Identify the preparation type.
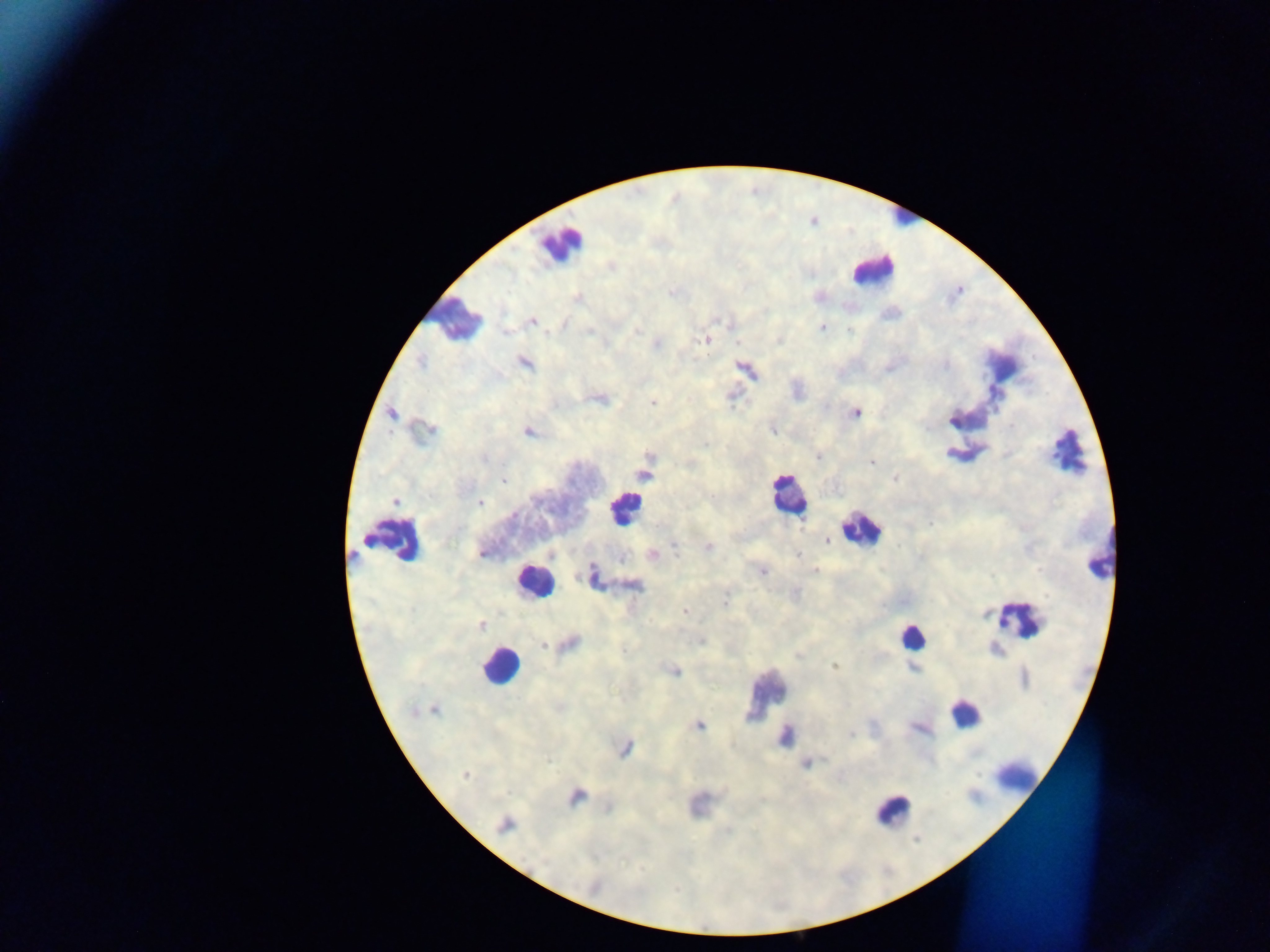

Thick blood film.

Approximate centers as (x, y) in pixels. Leukocyte locations: (554, 244), (864, 274), (455, 320), (1066, 454), (786, 488), (866, 534), (406, 538), (533, 585), (912, 639), (492, 664), (760, 697), (964, 720), (1016, 777), (896, 815). Plasmodium parasite locations: (612, 267), (670, 292), (575, 298), (533, 322), (820, 328), (637, 329), (850, 330), (706, 340), (658, 344), (421, 362), (525, 363), (994, 392), (655, 402), (855, 414), (392, 415), (953, 421), (771, 430), (529, 434), (704, 445), (951, 454), (649, 456), (871, 463), (643, 473), (896, 478), (504, 481), (627, 499), (395, 501), (481, 504), (803, 524), (366, 539), (828, 540), (709, 546), (674, 549), (652, 553), (797, 554), (480, 555), (350, 558), (815, 568), (592, 572), (765, 572), (631, 584), (796, 594), (726, 596), (725, 601), (685, 611), (1004, 621), (482, 625), (700, 640), (571, 643), (544, 645), (798, 654), (834, 664), (913, 667), (676, 672), (436, 709), (701, 725), (923, 729), (852, 733), (786, 735), (627, 750), (548, 762), (806, 765), (466, 775), (574, 799), (607, 810), (502, 826), (728, 832), (624, 861), (643, 868), (674, 892). Image is 1270×952 pixels. Single field of view. Collected in Ghana. Photographed through a microscope with a mobile-phone camera.